State which parasite is depicted.
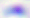
Toxoplasma gondii.

modality = micrograph
magnification = 400x